Assess this cell for malaria.
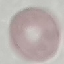
Uninfected.

stain = Giemsa
preparation = thin blood smear
capture = smartphone through the microscope eyepiece
image type = cell patch, automatically extracted from a larger field of view and resized to 64 × 64 pixels